Name the blood parasite species.
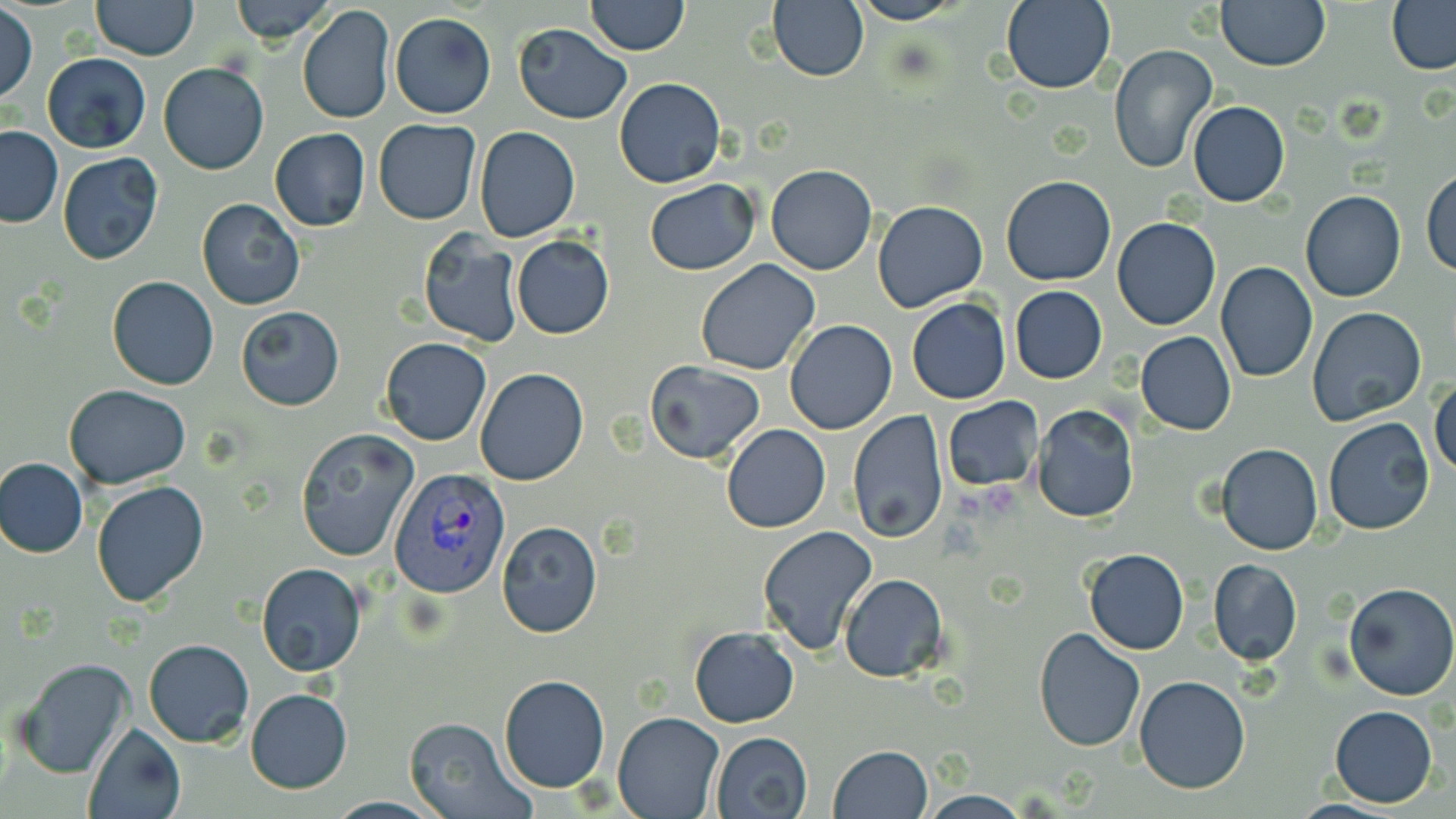

Plasmodium vivax.

Summary:
  - Coordinate format: approximate bounding boxes as (x1,y1)-(x2,y2) corner pairs in pixels
  - Platelet locations: (987,482)-(1023,518), (952,493)-(986,523)
  - Plasmodium vivax-infected red blood cell locations: (388,468)-(510,598)
  - Uninfected red blood cell locations: (91,0)-(198,60), (228,0)-(336,44), (584,0)-(689,55), (847,0)-(962,25), (999,0)-(1116,93), (1215,0)-(1329,70), (1386,1)-(1456,74), (765,2)-(871,82), (296,4)-(395,125), (533,4)-(681,85), (1,6)-(37,103), (389,12)-(496,119), (512,24)-(630,124), (1108,43)-(1218,176), (42,52)-(150,153), (157,62)-(270,175), (613,78)-(726,188), (1187,101)-(1291,207), (373,120)-(482,223), (0,126)-(63,228), (473,126)-(580,242), (269,128)-(370,231), (58,152)-(163,265), (766,165)-(877,276), (1422,169)-(1456,277), (1002,175)-(1116,286), (643,179)-(762,275), (1300,191)-(1405,302), (196,196)-(305,311), (873,201)-(989,315), (1112,216)-(1221,330), (418,233)-(524,348), (510,235)-(615,339), (695,258)-(821,375), (1215,263)-(1318,383), (106,277)-(219,390), (1011,287)-(1107,383), (906,299)-(1012,404), (235,305)-(344,411), (1307,307)-(1428,428), (785,319)-(897,434), (1135,331)-(1236,435), (799,334)-(928,494), (380,337)-(491,446), (647,360)-(766,464), (475,367)-(589,486), (1430,377)-(1456,478), (65,384)-(192,490), (942,397)-(1042,492), (1033,405)-(1139,523), (848,410)-(949,541), (1323,416)-(1435,535), (720,423)-(832,533), (293,429)-(418,562), (1216,443)-(1323,555), (1,458)-(88,558), (92,481)-(210,609), (496,521)-(603,638), (757,524)-(878,655), (1083,547)-(1189,655), (1208,558)-(1303,666), (256,564)-(368,678), (839,573)-(947,681), (1341,582)-(1456,701), (688,626)-(800,728), (1032,627)-(1146,752), (143,637)-(254,747), (12,657)-(137,778), (498,674)-(611,793), (1134,674)-(1251,793), (246,688)-(352,794), (1330,706)-(1438,806), (613,710)-(723,818), (403,717)-(532,819), (82,722)-(186,819), (709,731)-(813,819), (827,745)-(934,819), (917,792)-(1034,819)
  - Image size: 1456×819 pixels
  - Preparation: thin blood film
  - Field of view: one of a larger specimen
  - Magnification: 1000x
  - Modality: light microscopy
  - Stain: May-Grünwald-Giemsa